Locate every blood parasite and identify its species.
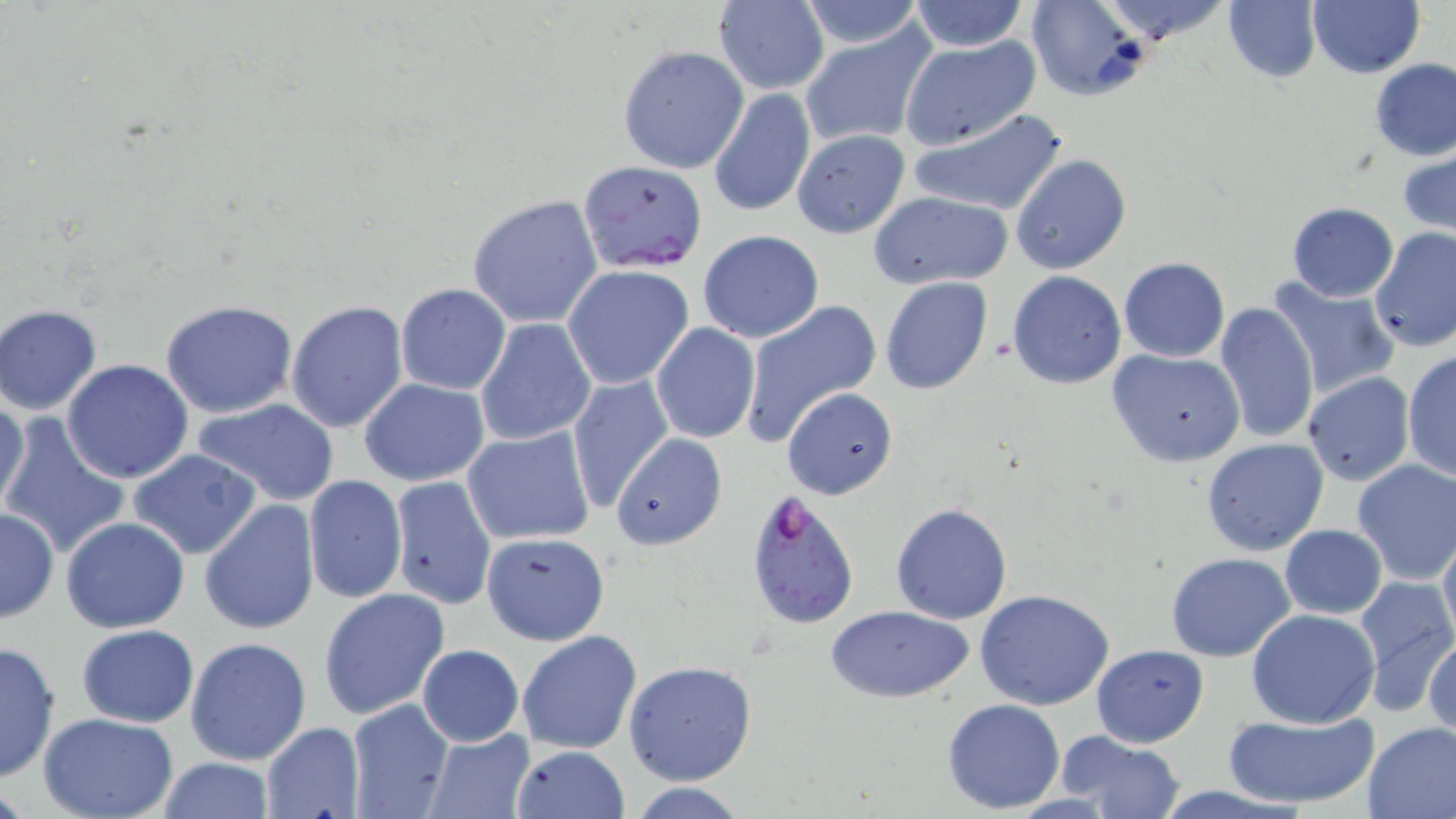
Approximate bounding boxes as (x1, y1, x2, y2) in pixels.
Plasmodium falciparum-infected red blood cells: (579, 159, 708, 273), (743, 484, 861, 633).
No Plasmodium ovale, Plasmodium malariae, Plasmodium vivax, Babesia divergens, or Trypanosoma brucei observed.

Uninfected red blood cell locations: (712, 0, 830, 94), (1025, 0, 1148, 101), (1093, 0, 1235, 43), (1223, 0, 1320, 83), (1306, 0, 1425, 78), (795, 1, 927, 50), (906, 1, 1031, 52), (798, 26, 936, 149), (898, 36, 1042, 151), (617, 44, 749, 174), (1369, 58, 1456, 161), (707, 84, 814, 217), (912, 107, 1069, 217), (790, 128, 911, 238), (1398, 148, 1456, 237), (1010, 154, 1130, 274), (868, 190, 1014, 289), (465, 193, 605, 328), (1286, 201, 1399, 302), (1369, 226, 1456, 352), (697, 230, 824, 343), (1119, 256, 1230, 363), (561, 264, 696, 390), (1007, 271, 1126, 389), (1267, 275, 1400, 396), (880, 276, 994, 397), (395, 283, 510, 395), (158, 299, 301, 419), (738, 299, 880, 444), (1212, 299, 1318, 443), (285, 300, 410, 434), (0, 305, 102, 415), (476, 318, 596, 447), (650, 323, 761, 444), (1106, 348, 1246, 468), (1402, 351, 1456, 483), (62, 359, 194, 483), (1301, 373, 1414, 486), (568, 374, 674, 508), (358, 378, 490, 486), (781, 387, 899, 499), (1, 395, 29, 515), (194, 399, 341, 506), (0, 416, 132, 560), (462, 426, 596, 546), (611, 433, 726, 551), (1201, 437, 1329, 555), (128, 449, 260, 559), (1351, 459, 1456, 584), (302, 475, 407, 606), (389, 475, 496, 609), (199, 498, 321, 636), (890, 501, 1014, 624), (0, 508, 58, 623), (61, 516, 190, 634), (1280, 523, 1387, 619), (1437, 527, 1456, 646), (480, 531, 611, 645), (1166, 552, 1296, 660), (1352, 576, 1456, 707), (319, 588, 452, 722), (974, 590, 1115, 711), (825, 604, 973, 703), (1246, 607, 1381, 728), (76, 624, 199, 728), (516, 629, 642, 756), (1424, 631, 1456, 744), (185, 636, 312, 766), (0, 639, 60, 782), (1091, 643, 1209, 748), (416, 645, 524, 747), (624, 660, 757, 787), (942, 698, 1066, 814), (345, 699, 455, 819), (1222, 710, 1378, 810), (38, 712, 181, 819), (1361, 720, 1456, 819), (260, 722, 364, 817), (425, 728, 536, 817), (1055, 730, 1185, 818), (511, 745, 628, 818), (153, 756, 279, 819). Slide-level diagnosis: Plasmodium falciparum. 1000x magnification. Light microscopy. Image is 1456×819 pixels. Single field of view. May-Grünwald-Giemsa stain. Thin blood film.